Assess this cell for malaria.
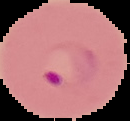

It is parasitized.

Summary:
  - Image size: 130×121 pixels
  - Image type: segmented cell region with the area outside set to black
  - Preparation: thin blood film